Identify the parasite.
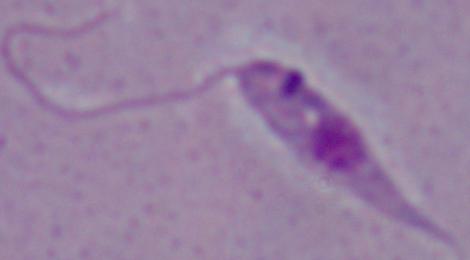

This is Leishmania.

Summary:
  - Magnification: 1000x
  - Modality: micrograph